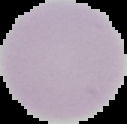

Image is 127×124 pixels. Cell region segmented out of the field of view; the surrounding area is masked to black. Malaria status: uninfected. From a thin blood film.